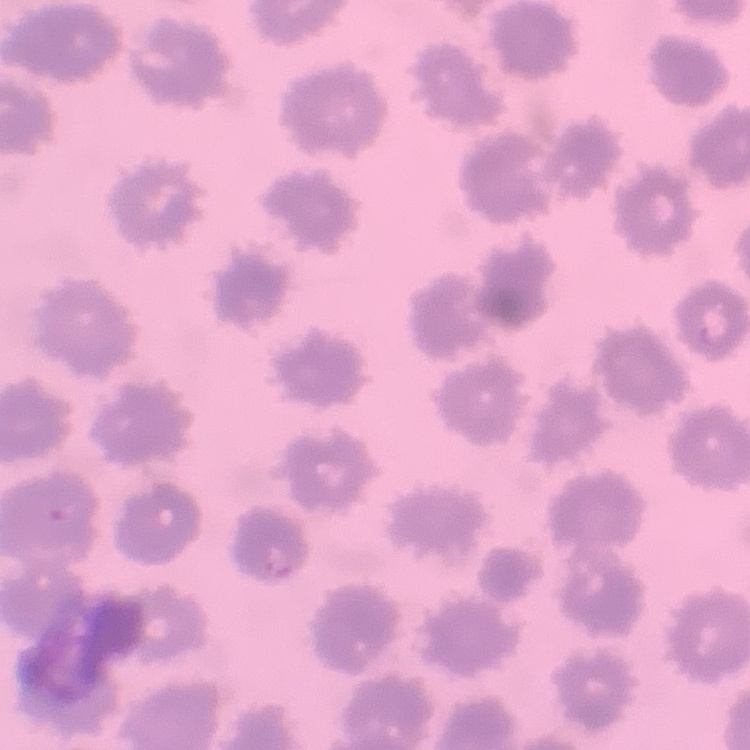 The red blood cells show no rouleaux formation. Thin blood film. Square crop of a larger photomicrograph. Stained with either Field's or Giemsa.